Report the malaria status of this cell.
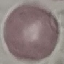

It is uninfected.

stain = Giemsa
image type = automatically extracted cell patch, resized to 64 × 64 pixels
preparation = thin blood film
capture = smartphone camera at the microscope eyepiece